Evaluate for malaria.
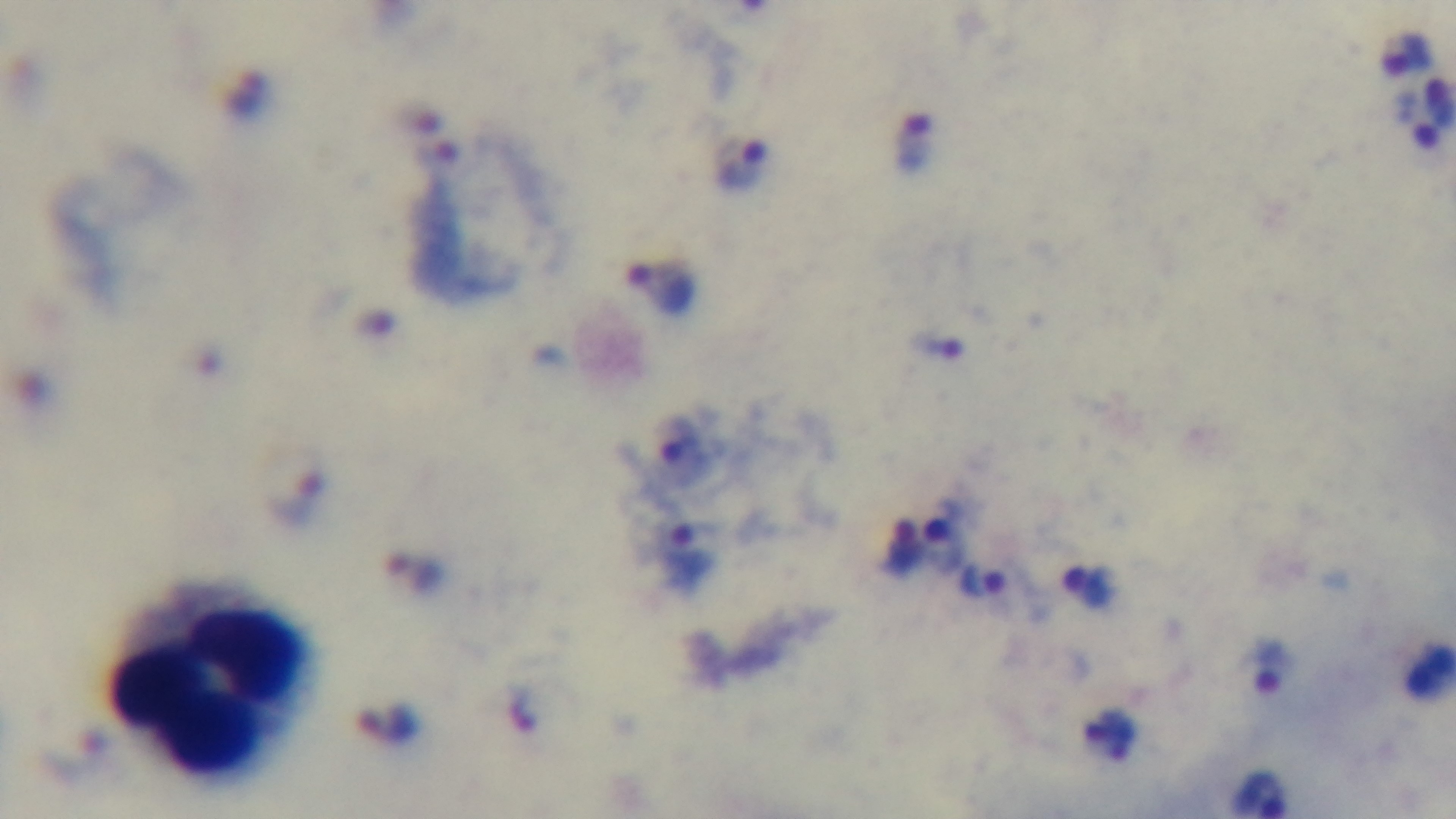
Positive.

Summary:
  - Modality: light microscopy
  - Stain: Giemsa
  - Capture: mounted 4K digital camera
  - Field of view: one from the slide
  - Objective: 100x oil immersion
  - Preparation: thick blood film